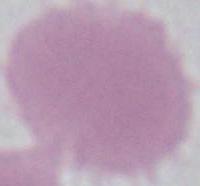

magnification = 1000x
identification = erythrocyte
modality = photomicrograph